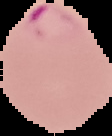

result = malaria parasites identified
image type = segmented cell region with the area outside set to black
preparation = thin blood smear
image size = 112×136 pixels